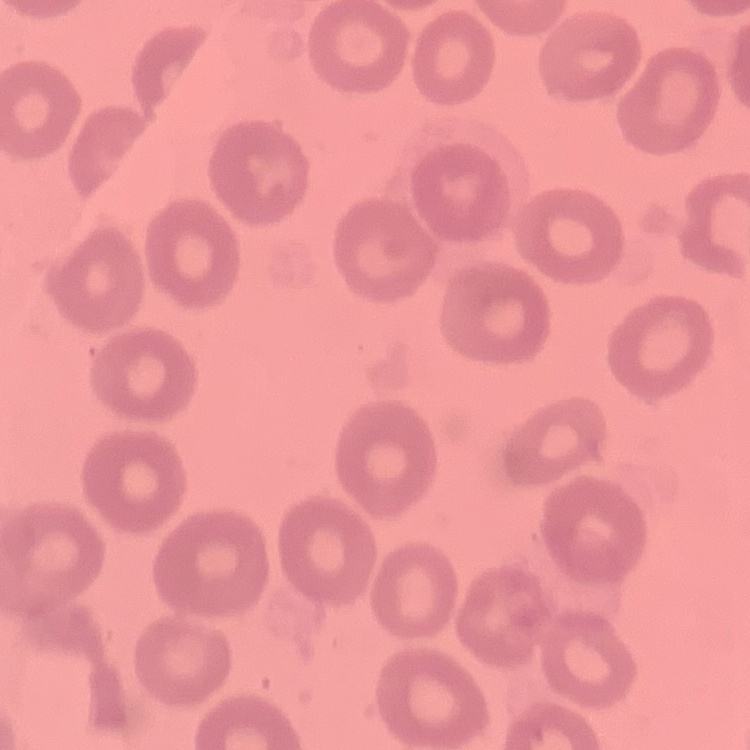 The erythrocytes exhibit no rouleaux formation. Thin peripheral smear. One tile cut from a larger photomicrograph. Field's or Giemsa stain.